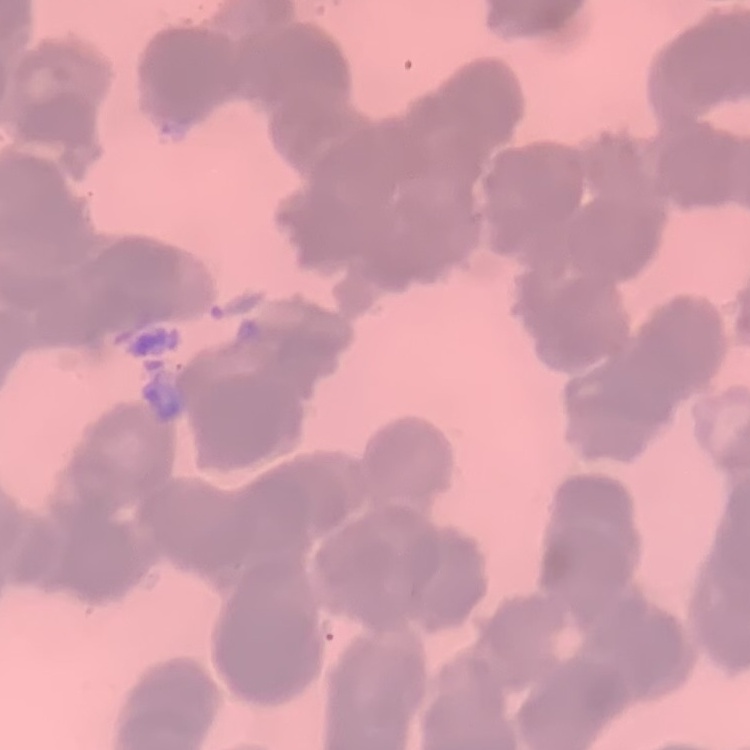

The erythrocytes exhibit rouleaux formation. One tile cut from a larger photomicrograph. Field's or Giemsa stain. Thin peripheral smear.